Locate and identify every blood parasite.
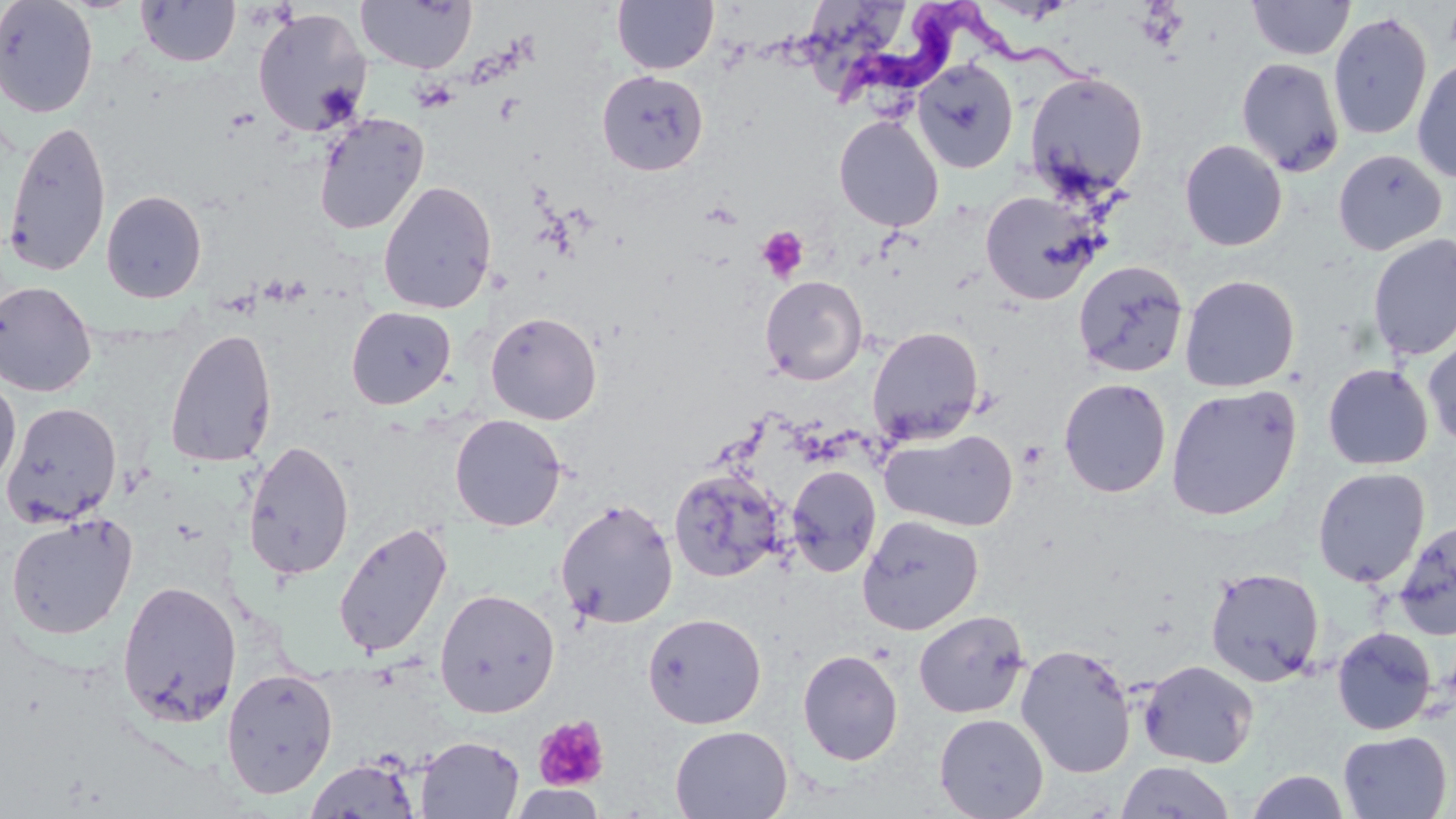
Approximate bounding boxes as (x1,y1)-(x2,y2) corner pairs in pixels.
Trypanosoma brucei: (826,2)-(1111,108).
No Plasmodium falciparum, Plasmodium ovale, Plasmodium malariae, Plasmodium vivax, or Babesia divergens observed.

slide_level_diagnosis: Trypanosoma brucei
preparation: thin blood smear
image_size: 1456×819 pixels
modality: optical microscopy
field_of_view: one of a larger specimen
uninfected_red_blood_cell_locations: 'approximate bounding boxes as (x1,y1)-(x2,y2) corner pairs in pixels: (0,0)-(98,118), (611,0)-(719,74), (807,0)-(908,94), (1247,0)-(1355,61), (136,1)-(241,67), (356,1)-(477,73), (252,7)-(372,137), (1328,11)-(1433,141), (1411,56)-(1456,183), (1235,57)-(1345,177), (911,58)-(1018,174), (596,70)-(708,175), (1024,70)-(1150,199), (313,112)-(430,236), (834,115)-(944,232), (2,118)-(113,278), (1179,139)-(1288,251), (1332,148)-(1447,256), (377,180)-(497,314), (101,190)-(207,303), (980,190)-(1104,306), (1367,233)-(1456,361), (1073,259)-(1190,378), (1179,274)-(1300,392), (760,275)-(868,385), (0,280)-(97,398), (346,306)-(456,410), (485,311)-(602,425), (867,325)-(984,445), (165,328)-(279,468), (1422,333)-(1456,450), (1323,363)-(1433,470), (0,377)-(21,490), (1059,378)-(1172,498), (1165,384)-(1302,521), (2,401)-(122,527), (449,414)-(567,532), (880,428)-(1019,532), (242,440)-(355,582), (785,466)-(881,578), (1312,467)-(1430,587), (669,468)-(787,582), (555,498)-(677,629), (5,514)-(137,639), (857,515)-(983,635), (1392,519)-(1456,640), (333,521)-(452,660), (1205,567)-(1325,687), (117,580)-(242,727), (434,588)-(560,718), (913,610)-(1029,719), (642,613)-(767,729), (1332,626)-(1437,735), (1015,644)-(1138,779), (797,649)-(904,766), (1138,659)-(1259,769), (221,668)-(338,799), (934,713)-(1049,819), (670,725)-(793,819), (1337,730)-(1453,818), (416,735)-(525,818), (304,757)-(421,818), (1115,761)-(1237,819), (1246,770)-(1350,819), (509,784)-(606,819)'
stain: May-Grünwald-Giemsa
platelet_locations: 'approximate bounding boxes as (x1,y1)-(x2,y2) corner pairs in pixels: (756,226)-(809,282), (533,715)-(610,792)'
magnification: 1000x